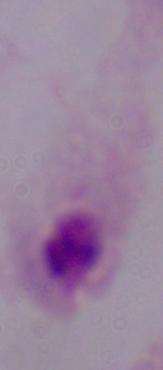
Summary:
  - Modality: photomicrograph
  - Magnification: 1000x
  - Identification: trichomonad